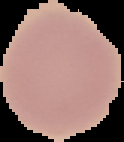
Malaria status: uninfected. Image is 124×142 pixels. Cell region segmented out of the field of view; the surrounding area is masked to black. From a thin blood smear.